State which parasite is depicted.
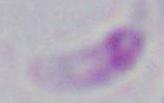

Toxoplasma gondii.

Micrograph. 1000x magnification.